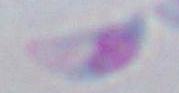

Summary:
  - Identification: Toxoplasma gondii
  - Modality: photomicrograph
  - Magnification: 1000x